Comment on the morphology of the erythrocytes.
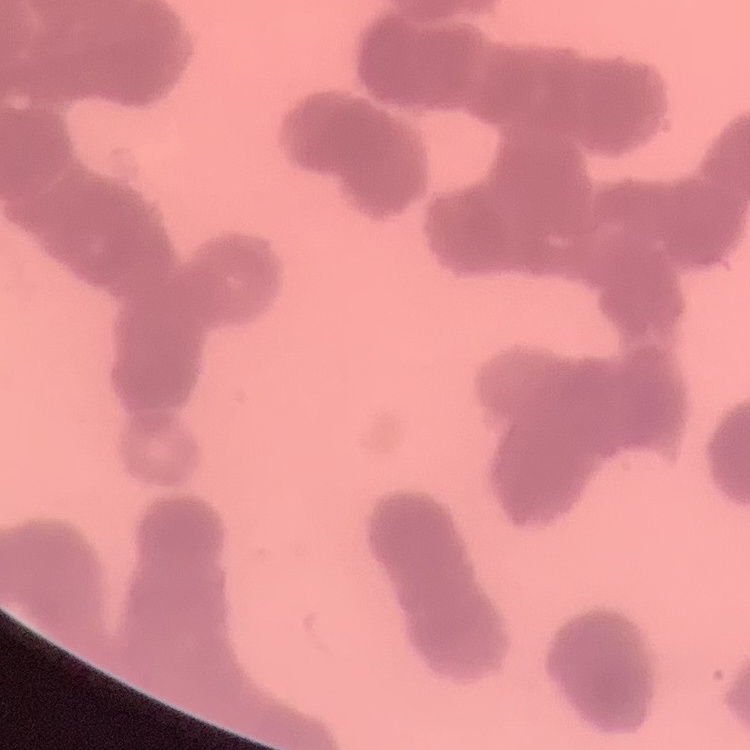

Rouleaux formation.

Thin blood smear. One tile cut from a larger photomicrograph. Stained with either Field's or Giemsa.